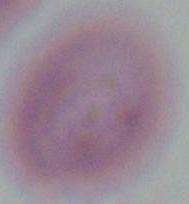

Captured at 1000x magnification. Micrograph. An erythrocyte is shown.